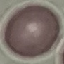
Summary:
  - Result: no malaria parasites detected
  - Capture: smartphone camera at the microscope eyepiece
  - Image type: automatically extracted cell patch, resized to 64 × 64 pixels
  - Preparation: thin smear
  - Stain: Giemsa